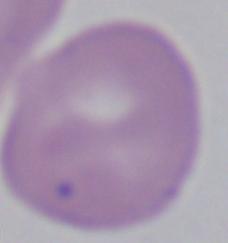
Summary:
  - Modality: photomicrograph
  - Magnification: 1000x
  - Identification: Babesia